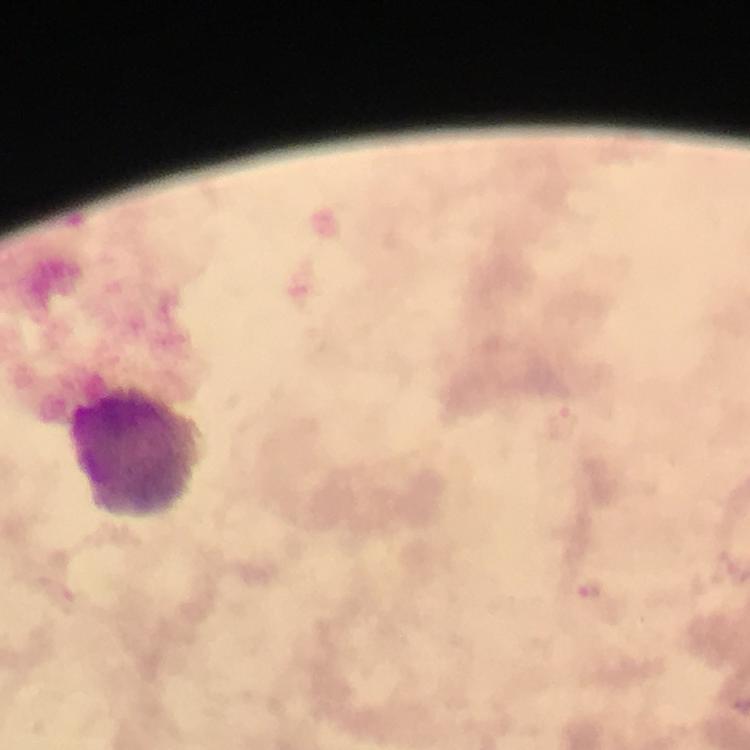
plasmodium_parasite_locations: 'approximate centers as (x, y) in pixels: (592, 590)'
preparation: thick blood film
stain: Giemsa
magnification: 100x
leukocyte_locations: 'approximate centers as (x, y) in pixels: (137, 455)'
capture: smartphone mounted on the microscope
cropped_from: one field of view
context: from a diagnostic examination for malaria
image_size: 750×750 pixels
immersion_oil: used